Assess this cell for malaria.
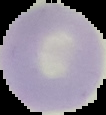
Uninfected.

Summary:
  - Preparation: thin blood film
  - Image type: cell region segmented out of the field of view; surrounding area masked to black
  - Image size: 106×115 pixels